Assess this cell for malaria.
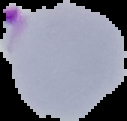

Parasitized.

image_type: segmented cell region with the area outside set to black
preparation: thin blood smear
image_size: 127×121 pixels